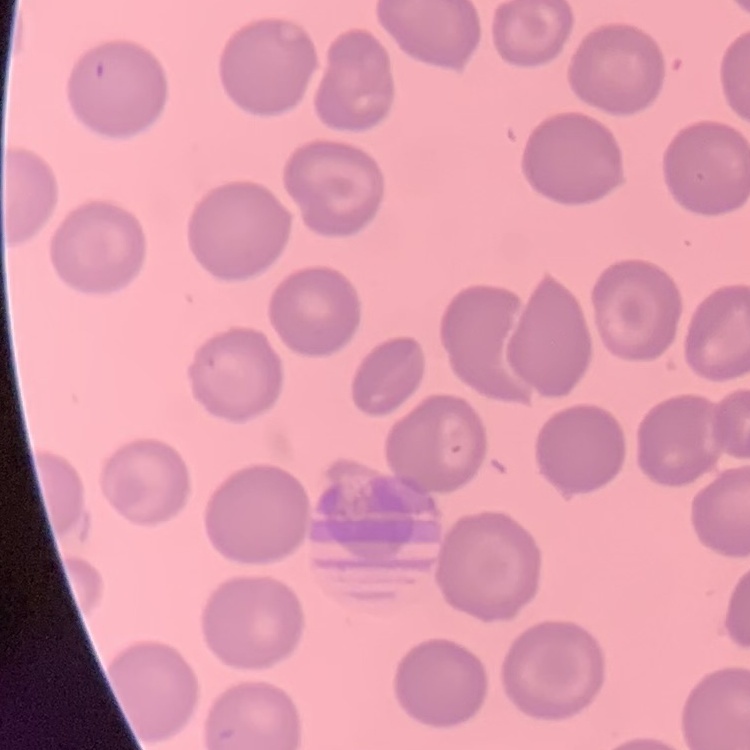
The red blood cells exhibit no rouleaux formation. Thin blood film. Field's or Giemsa stain. One tile cut from a larger photomicrograph.